Locate and identify every blood parasite.
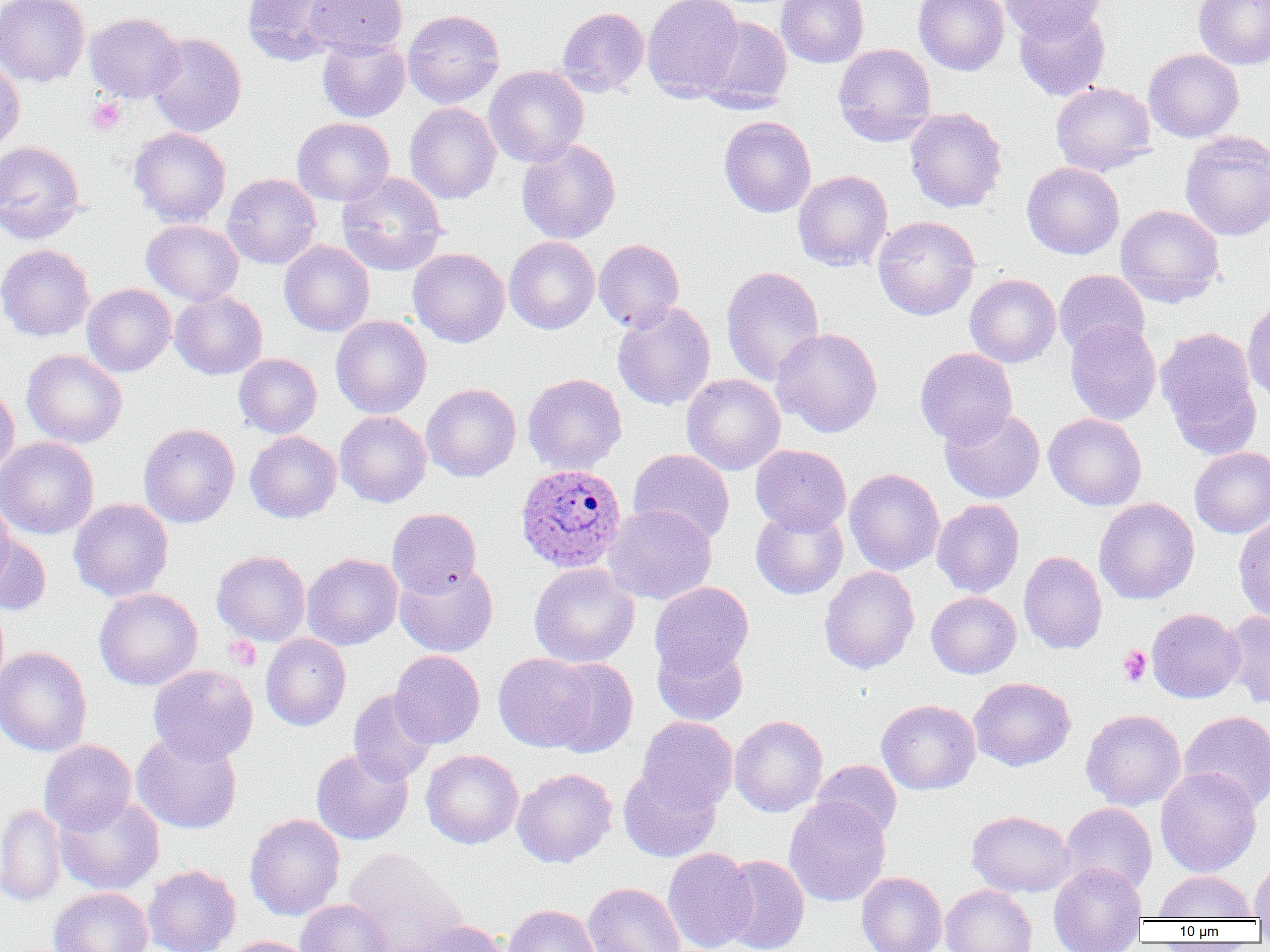

Approximate bounding boxes as (x1,y1)-(x2,y2) corner pairs in pixels.
Plasmodium ovale-infected red blood cells: (515,463)-(627,572).
No Plasmodium falciparum, Plasmodium malariae, Plasmodium vivax, Babesia divergens, or Trypanosoma brucei observed.

Platelet locations: (87,98)-(126,136), (224,636)-(261,670), (1118,645)-(1152,687). Uninfected red blood cell locations: (0,0)-(90,87), (241,0)-(347,66), (303,0)-(408,59), (642,0)-(744,101), (776,0)-(869,68), (913,0)-(1010,76), (1002,0)-(1107,42), (1193,0)-(1270,69), (1014,6)-(1110,101), (556,7)-(649,97), (403,9)-(505,109), (84,12)-(185,103), (699,16)-(793,112), (147,33)-(247,137), (317,37)-(410,123), (833,43)-(936,146), (1143,49)-(1244,143), (0,57)-(25,157), (484,65)-(589,167), (1050,81)-(1156,176), (404,102)-(501,204), (904,107)-(1007,213), (718,115)-(816,218), (291,117)-(395,206), (128,127)-(231,228), (1179,130)-(1270,241), (517,139)-(621,244), (0,140)-(86,243), (1021,162)-(1125,260), (793,170)-(893,271), (336,171)-(448,276), (222,173)-(321,269), (1115,205)-(1225,307), (873,216)-(980,321), (141,220)-(244,305), (504,236)-(600,334), (593,238)-(684,331), (279,240)-(375,337), (0,243)-(95,341), (407,247)-(510,347), (721,265)-(825,387), (1054,270)-(1149,358), (964,274)-(1061,367), (82,283)-(176,377), (170,291)-(267,379), (1243,297)-(1270,410), (612,300)-(716,411), (330,315)-(432,419), (1065,320)-(1161,425), (1156,326)-(1262,459), (771,327)-(883,437), (914,347)-(1017,446), (22,349)-(127,448), (233,353)-(322,438), (522,373)-(627,475), (682,374)-(785,475), (0,382)-(19,479), (421,383)-(521,482), (939,407)-(1045,503), (335,411)-(431,507), (1043,413)-(1147,510), (138,423)-(240,528), (245,431)-(342,523), (0,436)-(99,539), (750,443)-(851,535), (1189,447)-(1270,538), (628,449)-(735,545), (845,468)-(945,576), (0,496)-(15,593), (69,498)-(174,602), (1094,498)-(1200,604), (932,499)-(1024,597), (603,505)-(717,606), (750,505)-(848,600), (387,507)-(482,598), (1233,513)-(1270,624), (0,534)-(52,615), (212,550)-(311,646), (1019,551)-(1107,654), (302,553)-(403,650), (394,562)-(498,657), (529,562)-(640,668), (818,566)-(920,674), (649,581)-(754,676), (94,588)-(202,691), (926,591)-(1021,679), (1147,608)-(1244,703), (1221,610)-(1270,710), (261,634)-(351,731), (652,637)-(749,726), (0,646)-(92,757), (390,650)-(485,748), (493,652)-(597,752), (545,657)-(639,758), (148,664)-(258,764), (969,676)-(1076,771), (348,689)-(439,785), (876,698)-(981,795), (1081,709)-(1186,811), (1180,710)-(1270,812), (729,714)-(828,817), (637,716)-(738,812), (131,731)-(243,834), (39,739)-(137,835), (311,748)-(413,845), (421,748)-(523,849), (811,760)-(902,841), (618,765)-(722,862), (1155,767)-(1262,877), (512,768)-(617,868), (55,795)-(164,895), (784,796)-(891,907), (1060,802)-(1157,896), (0,803)-(66,906), (966,810)-(1077,898), (245,813)-(346,921), (343,847)-(466,952), (662,847)-(757,952), (720,855)-(810,952), (1249,859)-(1270,921), (1048,862)-(1147,952), (142,864)-(241,952), (1154,870)-(1256,920), (856,872)-(947,952), (583,882)-(685,952), (941,884)-(1037,952), (48,887)-(153,952), (295,898)-(393,952), (501,904)-(601,952), (407,920)-(510,952), (223,936)-(318,952). Slide-level diagnosis: Plasmodium ovale. Image is 1270×952 pixels. 1000x magnification. One field of a larger specimen. Thin blood smear. Light microscopy.